Describe the morphology of the erythrocytes.
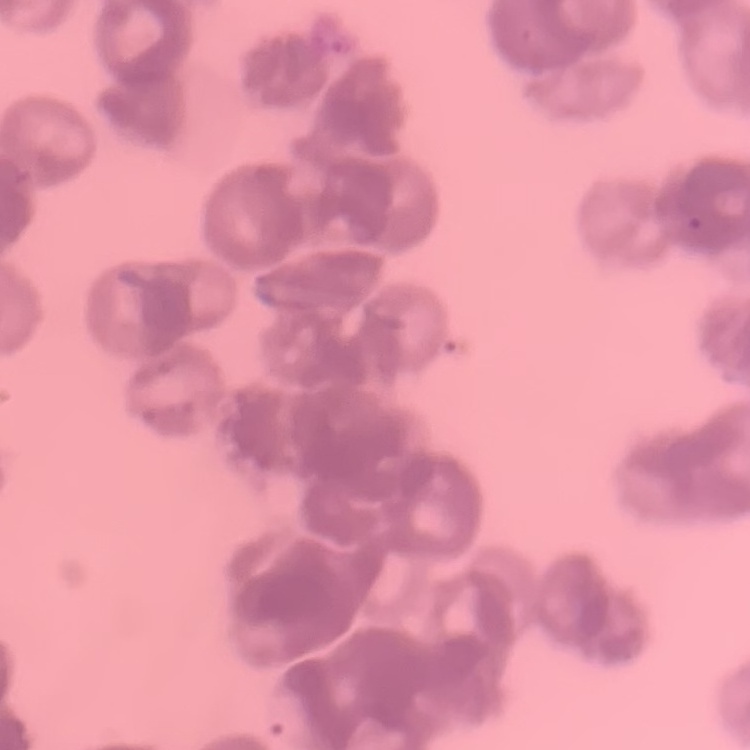
They show rouleaux formation.

stain = Field's or Giemsa
image type = one tile cut from a larger photomicrograph
preparation = thin blood film